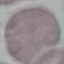

Summary:
  - Result: no malaria parasites seen
  - Preparation: thin blood smear
  - Stain: Giemsa
  - Image type: automatically extracted cell patch, resized to 64 × 64 pixels
  - Capture: smartphone through the microscope eyepiece